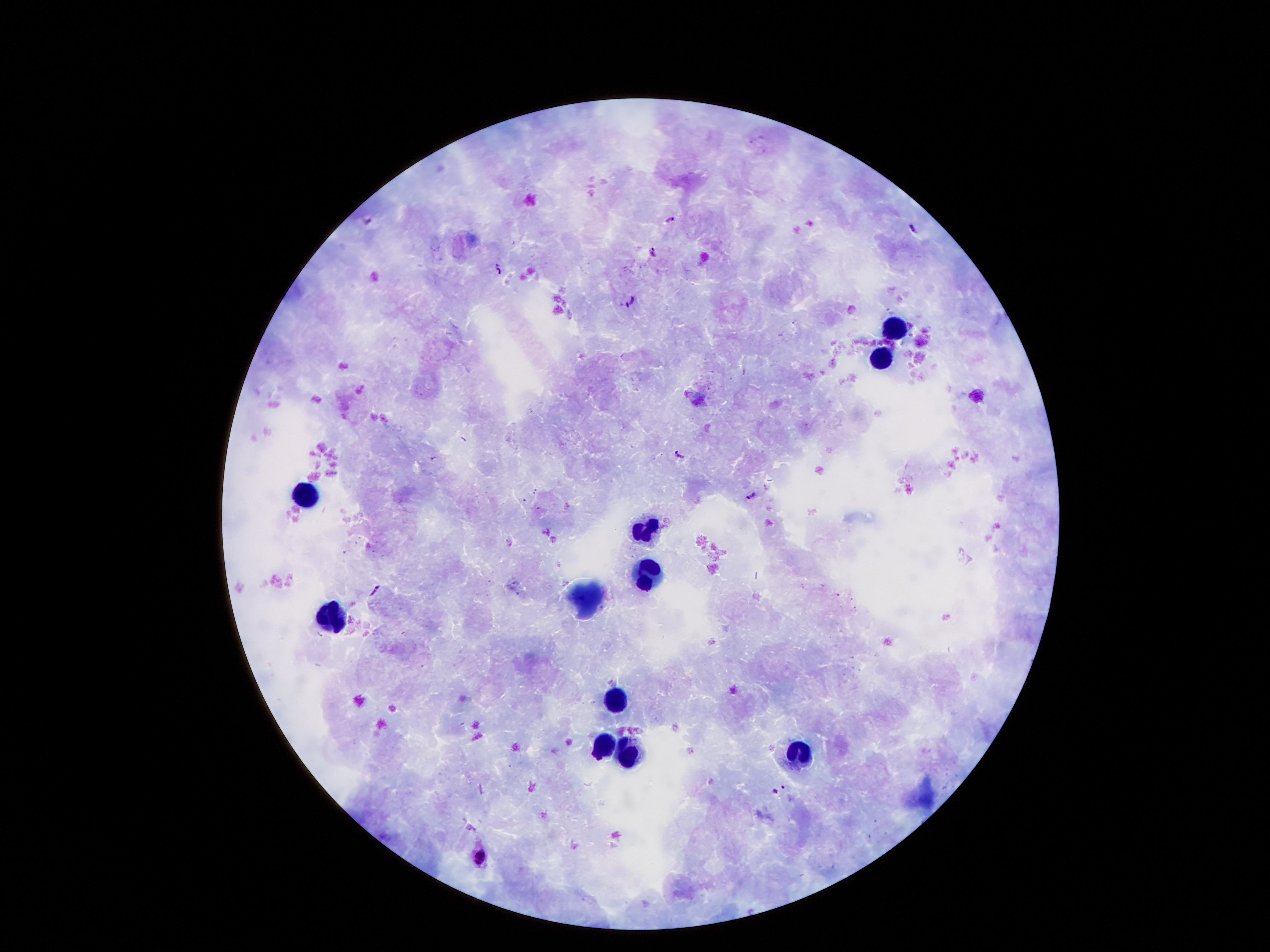
Approximate object centers, in pixels from the top-left corner.
Summary:
  - Leukocyte locations: (x=896, y=329), (x=879, y=364), (x=308, y=497), (x=647, y=532), (x=652, y=579), (x=330, y=621), (x=617, y=695), (x=602, y=747), (x=795, y=754), (x=627, y=757)
  - Plasmodium parasite locations: (x=668, y=220), (x=913, y=226), (x=654, y=254), (x=500, y=269), (x=633, y=302), (x=678, y=455), (x=748, y=496), (x=375, y=591), (x=776, y=791), (x=481, y=856)
  - Image size: 1270×952 pixels
  - Patient malaria status: infected with Plasmodium falciparum
  - Stain: Giemsa
  - Magnification: 100x
  - Capture: smartphone camera through the microscope eyepiece
  - Preparation: thick blood film
  - Field of view: single